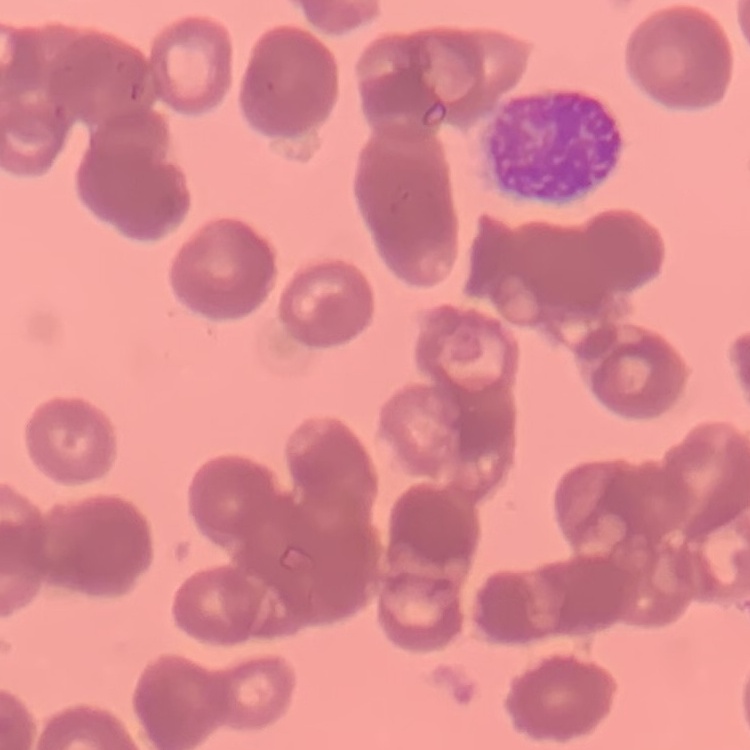

{
  "erythrocyte_morphology": "rouleaux formation",
  "image_type": "one tile cut from a larger photomicrograph",
  "stain": "Field's or Giemsa",
  "preparation": "thin peripheral smear"
}